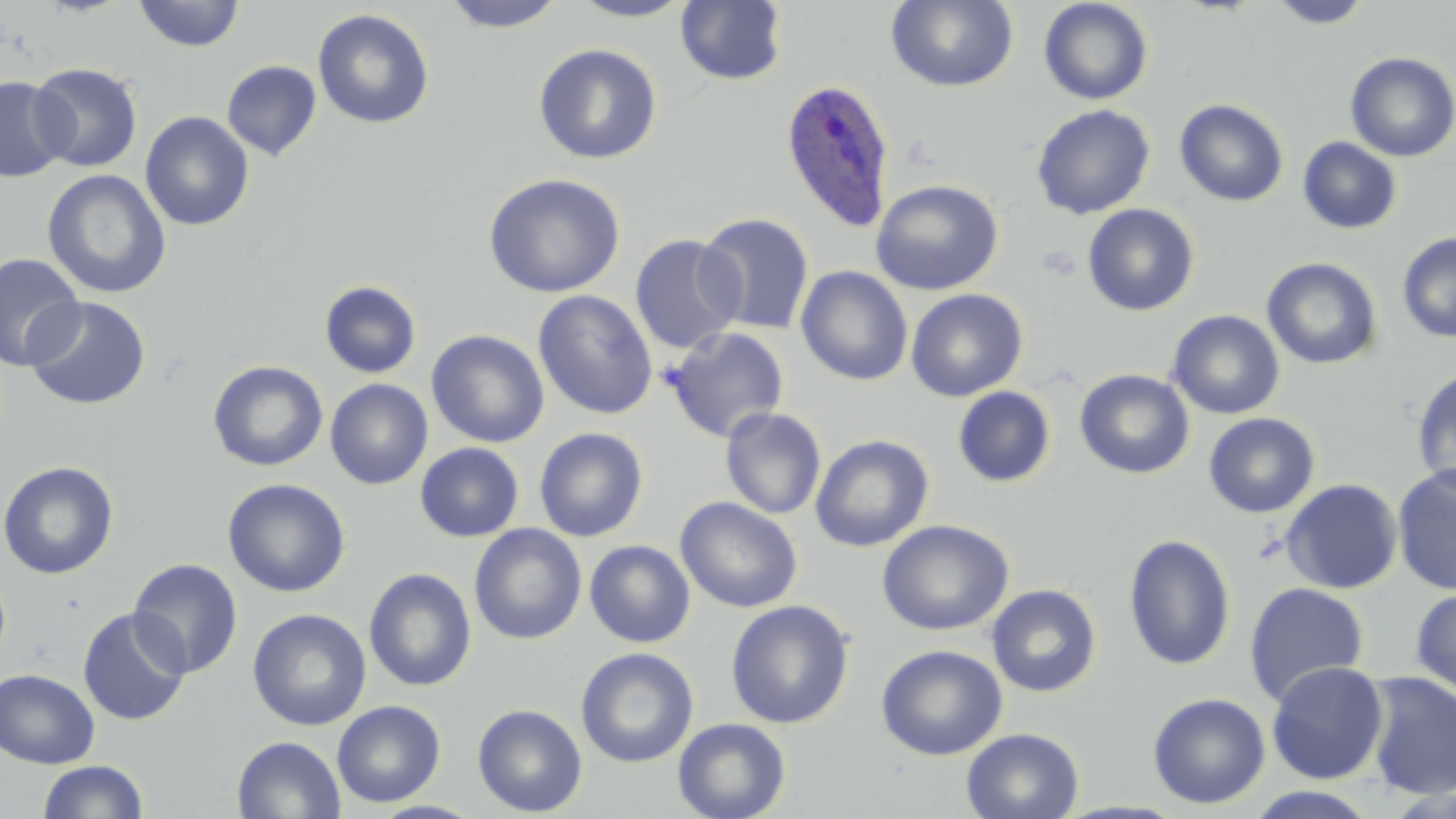

Summary:
  - Coordinate format: approximate bounding boxes as named x1/y1/x2/y2 corners in pixels
  - Uninfected red blood cell locations: (x1=441, y1=0, x2=568, y2=32), (x1=568, y1=0, x2=694, y2=22), (x1=675, y1=0, x2=787, y2=86), (x1=887, y1=0, x2=1018, y2=92), (x1=1038, y1=0, x2=1154, y2=105), (x1=133, y1=1, x2=245, y2=51), (x1=1267, y1=1, x2=1374, y2=28), (x1=312, y1=8, x2=435, y2=130), (x1=533, y1=43, x2=662, y2=164), (x1=1344, y1=52, x2=1456, y2=161), (x1=221, y1=60, x2=322, y2=161), (x1=28, y1=63, x2=143, y2=172), (x1=0, y1=76, x2=72, y2=182), (x1=1174, y1=98, x2=1289, y2=206), (x1=1031, y1=104, x2=1155, y2=220), (x1=140, y1=111, x2=254, y2=231), (x1=1298, y1=137, x2=1403, y2=235), (x1=42, y1=169, x2=172, y2=299), (x1=483, y1=173, x2=626, y2=298), (x1=870, y1=179, x2=1003, y2=296), (x1=1082, y1=204, x2=1200, y2=316), (x1=696, y1=212, x2=815, y2=335), (x1=1397, y1=232, x2=1456, y2=343), (x1=629, y1=234, x2=744, y2=354), (x1=1, y1=252, x2=85, y2=372), (x1=1262, y1=257, x2=1383, y2=370), (x1=795, y1=266, x2=913, y2=386), (x1=319, y1=280, x2=422, y2=378), (x1=905, y1=288, x2=1028, y2=402), (x1=532, y1=290, x2=658, y2=420), (x1=24, y1=296, x2=151, y2=410), (x1=1166, y1=309, x2=1285, y2=419), (x1=663, y1=326, x2=790, y2=444), (x1=426, y1=330, x2=550, y2=448), (x1=208, y1=360, x2=328, y2=471), (x1=1411, y1=365, x2=1456, y2=495), (x1=1074, y1=369, x2=1194, y2=479), (x1=325, y1=378, x2=433, y2=490), (x1=953, y1=386, x2=1056, y2=487), (x1=720, y1=407, x2=827, y2=520), (x1=1204, y1=413, x2=1320, y2=517), (x1=534, y1=427, x2=648, y2=542), (x1=810, y1=434, x2=934, y2=552), (x1=415, y1=442, x2=524, y2=542), (x1=0, y1=460, x2=119, y2=579), (x1=1393, y1=464, x2=1456, y2=597), (x1=222, y1=478, x2=351, y2=597), (x1=1280, y1=478, x2=1403, y2=594), (x1=675, y1=496, x2=802, y2=613), (x1=877, y1=519, x2=1014, y2=636), (x1=469, y1=523, x2=587, y2=645), (x1=1122, y1=533, x2=1236, y2=671), (x1=584, y1=539, x2=696, y2=648), (x1=127, y1=558, x2=243, y2=678), (x1=364, y1=567, x2=477, y2=692), (x1=1244, y1=582, x2=1370, y2=706), (x1=986, y1=584, x2=1102, y2=697), (x1=1411, y1=587, x2=1456, y2=699), (x1=726, y1=600, x2=854, y2=729), (x1=77, y1=607, x2=191, y2=726), (x1=247, y1=608, x2=371, y2=731), (x1=876, y1=644, x2=1007, y2=759), (x1=576, y1=647, x2=699, y2=768), (x1=1265, y1=660, x2=1389, y2=784), (x1=0, y1=668, x2=100, y2=768), (x1=1362, y1=671, x2=1456, y2=800), (x1=1147, y1=692, x2=1272, y2=809), (x1=332, y1=700, x2=445, y2=807), (x1=472, y1=703, x2=588, y2=817), (x1=672, y1=717, x2=791, y2=819), (x1=962, y1=727, x2=1084, y2=819), (x1=232, y1=735, x2=346, y2=818), (x1=37, y1=760, x2=148, y2=818), (x1=1243, y1=786, x2=1382, y2=819), (x1=368, y1=800, x2=488, y2=819)
  - Plasmodium ovale-infected red blood cell locations: (x1=779, y1=78, x2=895, y2=233)
  - Slide-level diagnosis: Plasmodium ovale
  - Stain: May-Grünwald-Giemsa
  - Preparation: thin blood film
  - Image size: 1456×819 pixels
  - Magnification: 1000x
  - Field of view: single
  - Modality: optical microscopy